Comment on the morphology of the erythrocytes.
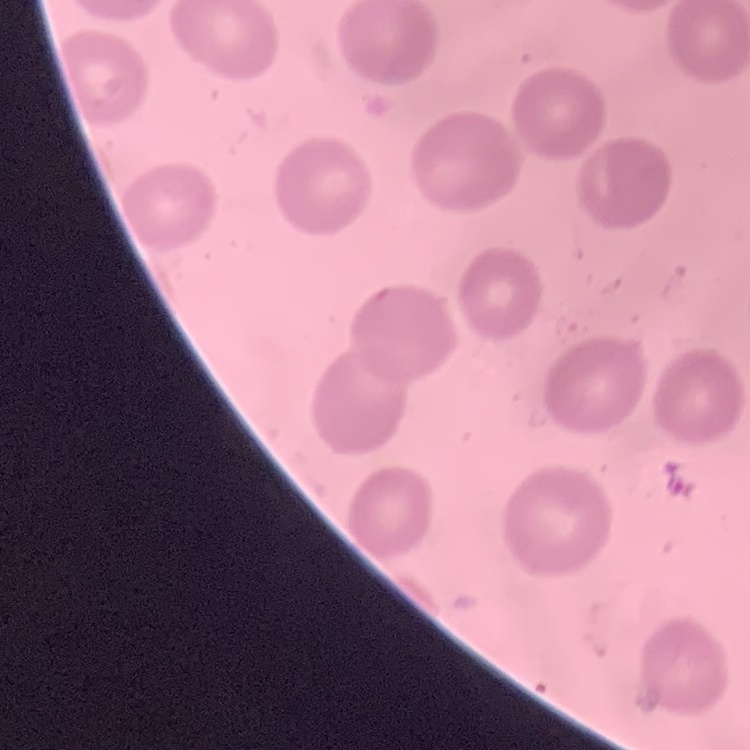

No rouleaux formation.

Square crop of a larger photomicrograph. Thin blood film. Field's or Giemsa stain.